Assess the morphology of the red blood cells.
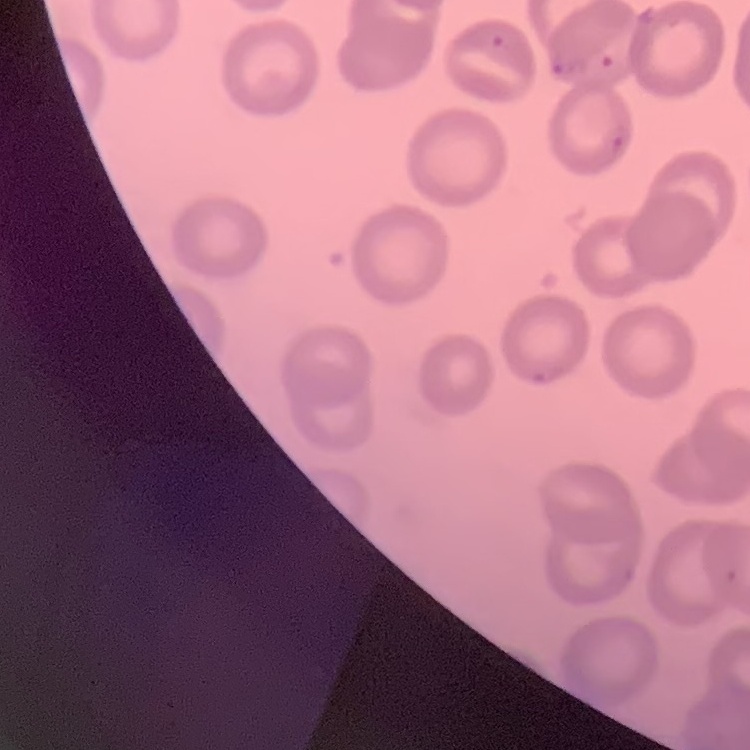
No rouleaux formation.

preparation: thin blood film
stain: Field's or Giemsa
image_type: square crop of a larger photomicrograph